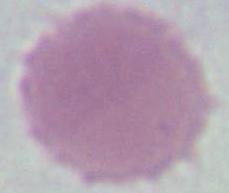 1000x magnification. An erythrocyte is seen. Micrograph.